Outline each blood parasite and name the species.
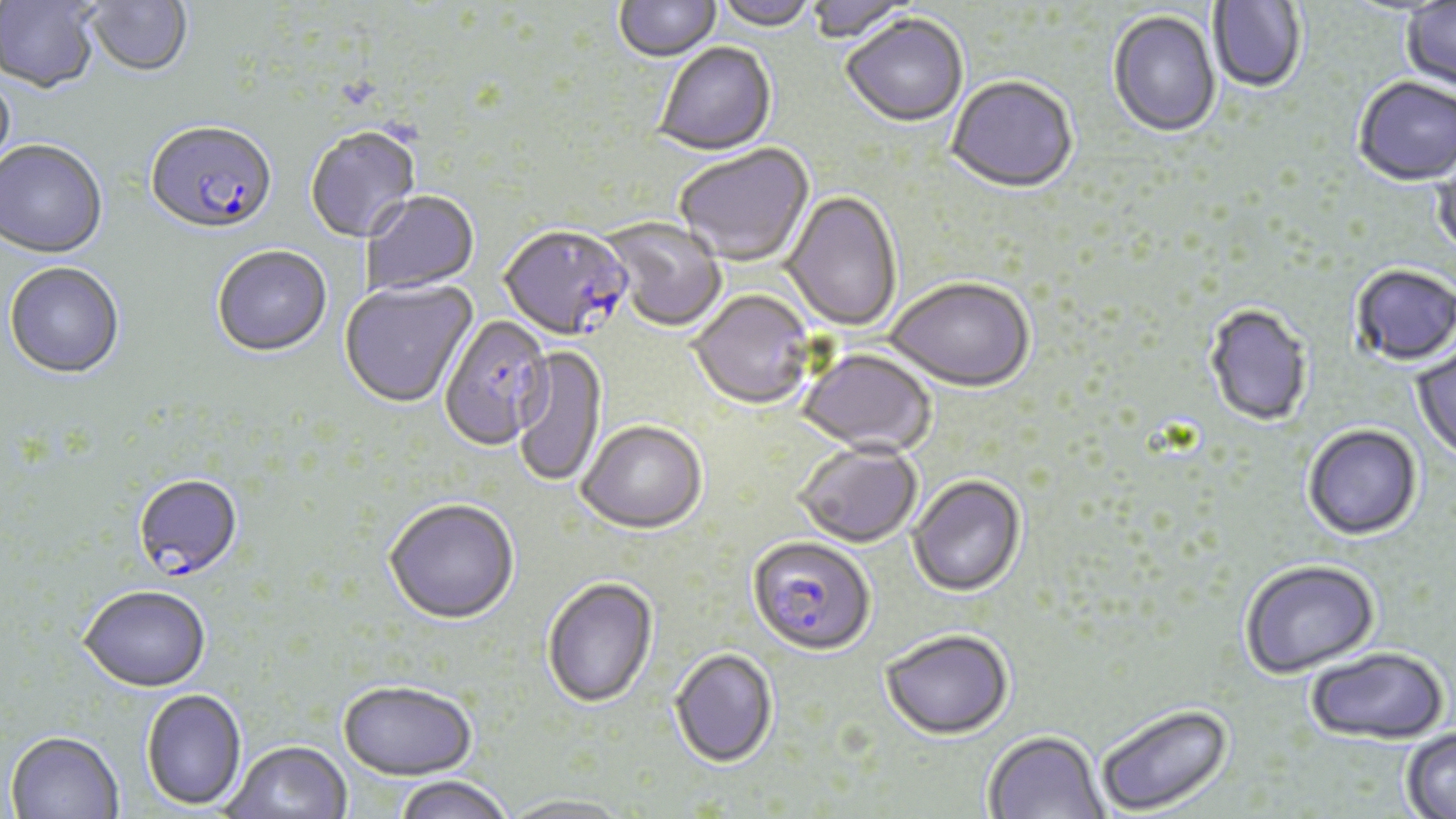
Approximate bounding boxes as [x1, y1, x2, y2] in pixels.
Plasmodium falciparum-infected red blood cells: [146, 124, 277, 239], [500, 227, 634, 343], [440, 316, 553, 452], [132, 475, 243, 582], [748, 537, 875, 658].
No Plasmodium ovale, Plasmodium malariae, Plasmodium vivax, Babesia divergens, or Trypanosoma brucei observed.

Uninfected red blood cell locations: [84, 0, 193, 79], [615, 0, 721, 64], [715, 0, 817, 33], [805, 0, 918, 44], [0, 1, 100, 94], [1209, 1, 1306, 94], [1401, 2, 1456, 94], [1108, 11, 1221, 140], [841, 16, 968, 129], [655, 44, 777, 158], [0, 69, 17, 181], [947, 78, 1078, 196], [1353, 79, 1456, 187], [305, 128, 422, 245], [0, 142, 108, 260], [674, 145, 815, 268], [1431, 149, 1456, 263], [361, 192, 480, 297], [782, 192, 902, 333], [601, 218, 727, 333], [212, 248, 332, 359], [4, 264, 125, 381], [1350, 266, 1456, 368], [886, 279, 1035, 395], [339, 280, 478, 410], [688, 292, 815, 412], [1204, 305, 1313, 428], [513, 345, 607, 488], [1410, 345, 1456, 465], [797, 349, 936, 458], [578, 422, 708, 536], [1303, 425, 1423, 542], [794, 444, 922, 549], [908, 477, 1026, 599], [384, 500, 519, 626], [1240, 561, 1380, 680], [542, 578, 658, 709], [78, 589, 211, 695], [880, 632, 1013, 743], [669, 649, 777, 768], [1305, 649, 1450, 748], [338, 681, 476, 782], [141, 690, 246, 812], [1096, 705, 1233, 816], [1401, 727, 1456, 819], [983, 733, 1107, 819], [5, 734, 124, 819], [225, 742, 352, 819], [393, 777, 513, 819], [500, 795, 635, 819]. Slide-level diagnosis: Plasmodium falciparum. Image is 1456×819 pixels. Thin blood smear. Light microscopy. 1000x magnification. One field of a larger specimen. May-Grünwald-Giemsa-stained preparation.